Assess this cell for malaria.
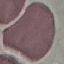

It is uninfected.

Summary:
  - Capture: smartphone through the microscope eyepiece
  - Stain: Giemsa
  - Preparation: thin blood film
  - Image type: automatically extracted cell patch, resized to 64 × 64 pixels